Assess for malaria.
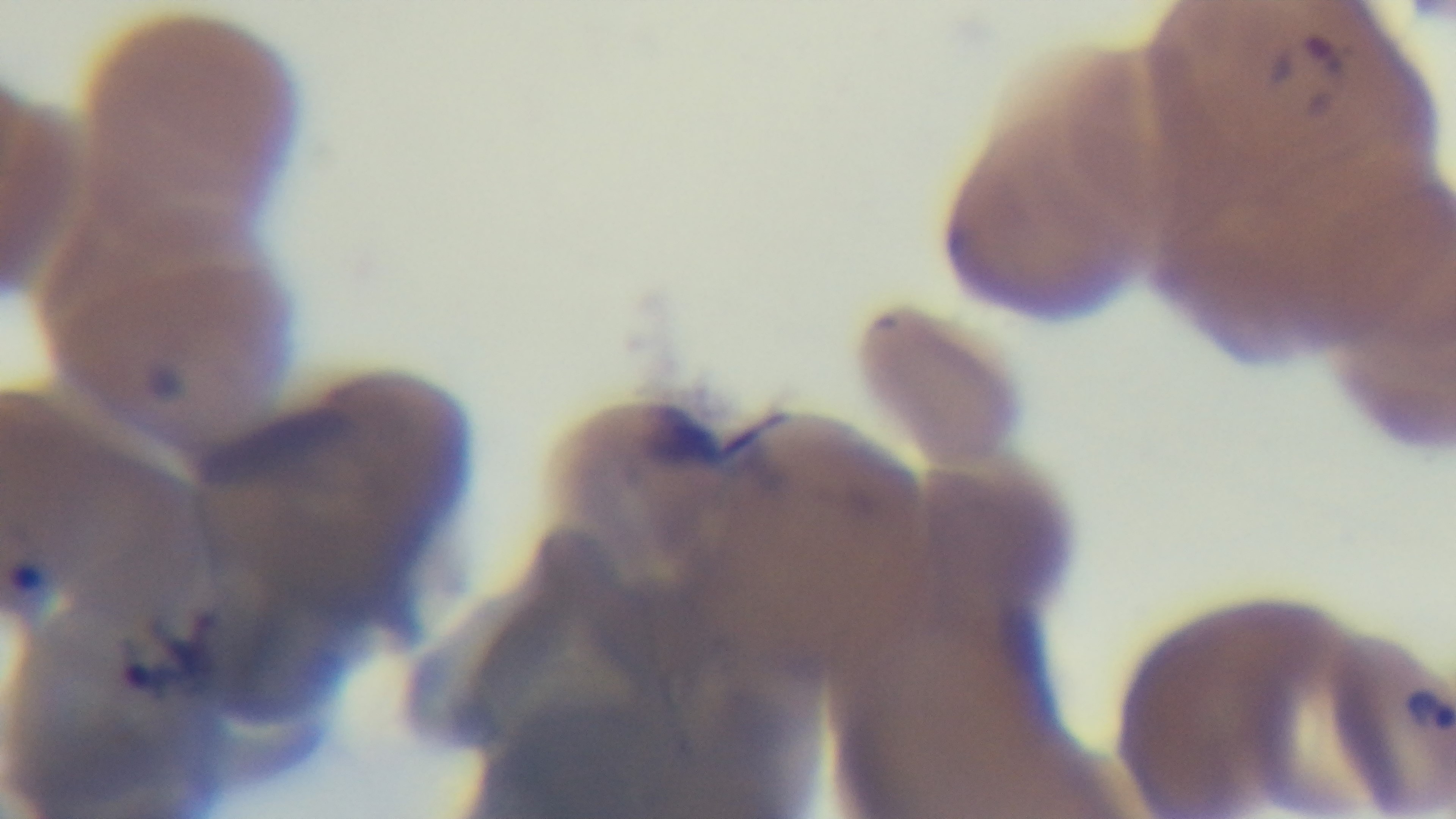
Infected.

field of view = single
capture = mounted 4K digital camera
modality = light microscopy
objective = 100x oil immersion
stain = Giemsa
preparation = thin